Report the malaria status of this cell.
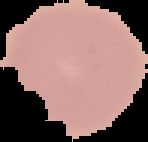

It is uninfected.

image size = 148×142 pixels
image type = segmented cell region on a black background
preparation = thin blood film